Report the malaria status of this cell.
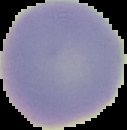
It is uninfected.

Summary:
  - Image size: 127×130 pixels
  - Preparation: thin blood smear
  - Image type: cell region segmented out of the field of view; surrounding area masked to black